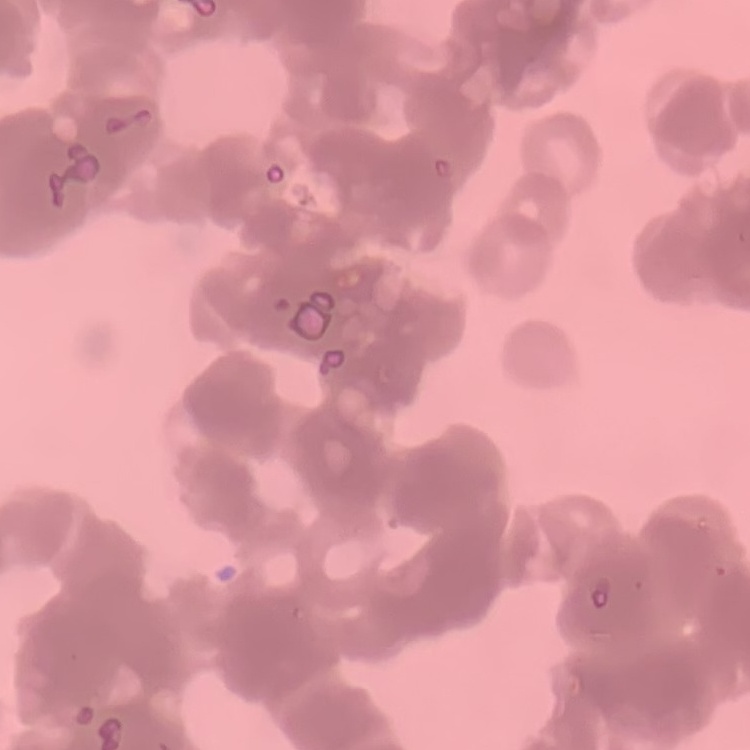

red_blood_cell_morphology: rouleaux formation
preparation: thin peripheral smear
image_type: one tile cut from a larger photomicrograph
stain: Field's or Giemsa